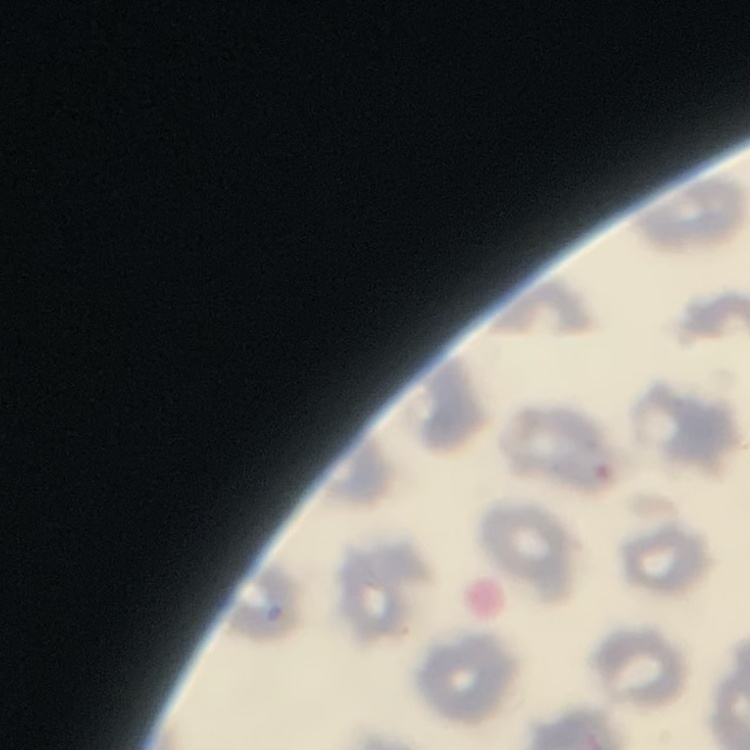
red blood cell morphology = no rouleaux formation
preparation = thin blood film
image type = one tile cut from a larger photomicrograph
stain = Field's or Giemsa